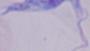 A trypanosome is seen. Photomicrograph. Captured at 1000x magnification.